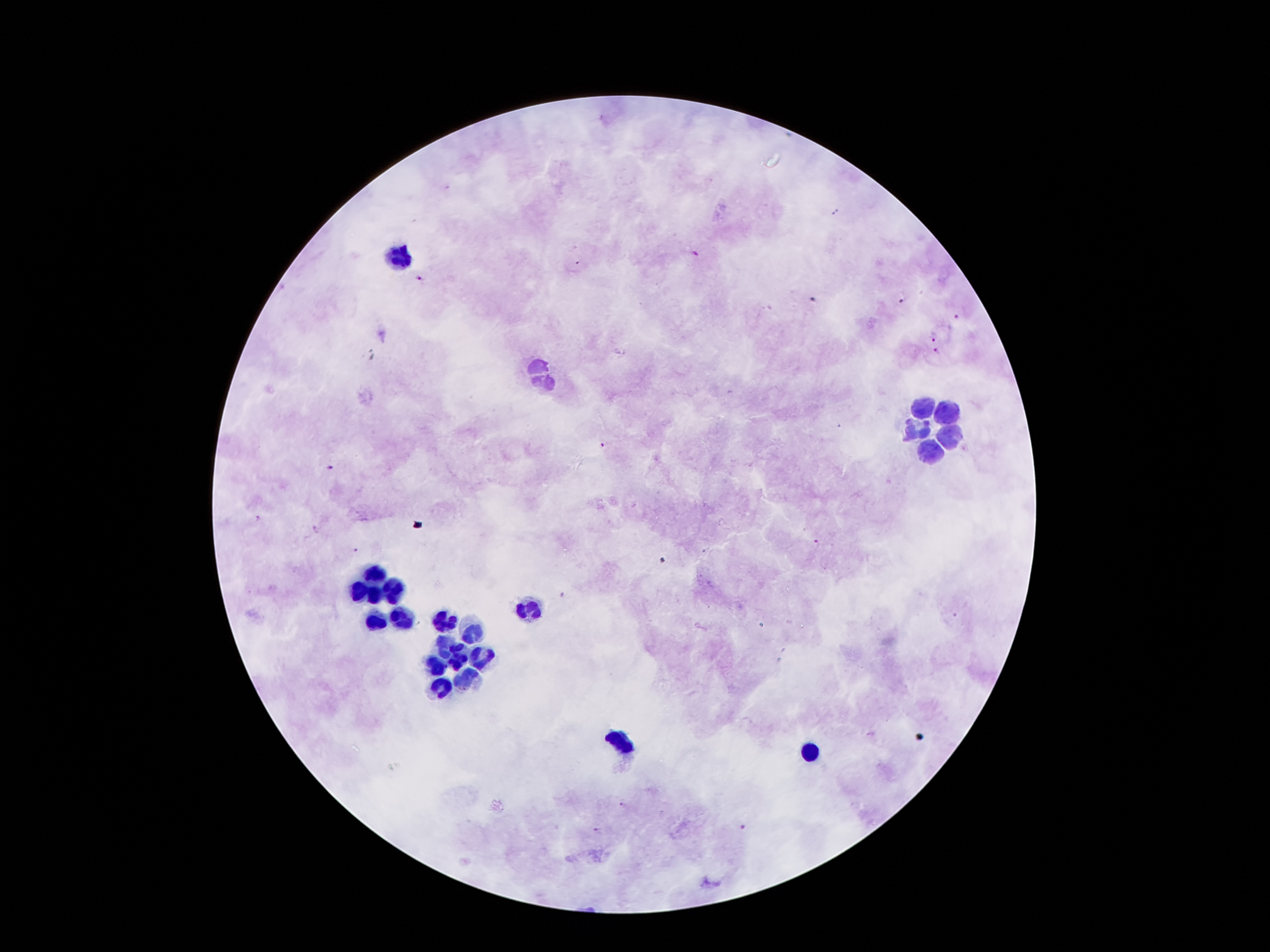

Approximate centers as [x, y] in pixels. Leukocyte locations: [399, 254], [539, 379], [920, 405], [947, 410], [915, 430], [947, 435], [930, 447], [371, 574], [393, 587], [360, 591], [375, 596], [529, 609], [398, 619], [444, 619], [375, 620], [475, 637], [440, 645], [482, 656], [455, 660], [437, 665], [467, 676], [442, 688], [622, 742], [809, 752]. Plasmodium parasite locations: [694, 254], [578, 265], [420, 277], [811, 299], [899, 301], [956, 317], [934, 340], [939, 353], [604, 445], [328, 467], [816, 539], [356, 550], [563, 595], [621, 804], [741, 828], [596, 830]. Smartphone photograph taken through the microscope eyepiece. Giemsa-stained preparation. Patient malaria status: positive for Plasmodium falciparum. Thick blood smear. Image is 1270×952 pixels. 100x magnification. Single field of view.